Name the parasite shown.
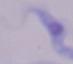
A trypanosome.

Captured at 1000x magnification. Photomicrograph.